Describe the morphology of the erythrocytes.
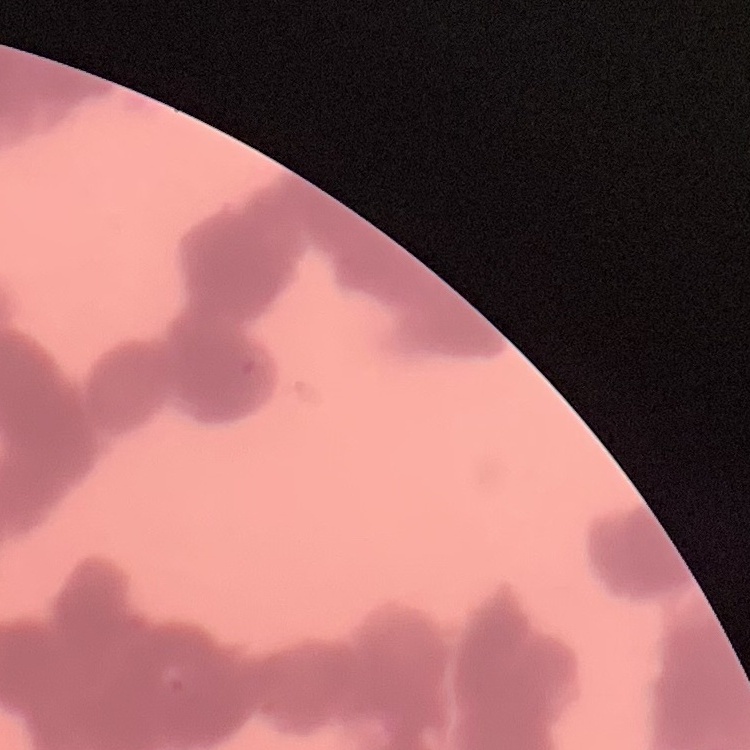

Rouleaux formation.

preparation: thin peripheral smear
stain: Field's or Giemsa
image_type: one tile cut from a larger photomicrograph